Assess the morphology of the erythrocytes.
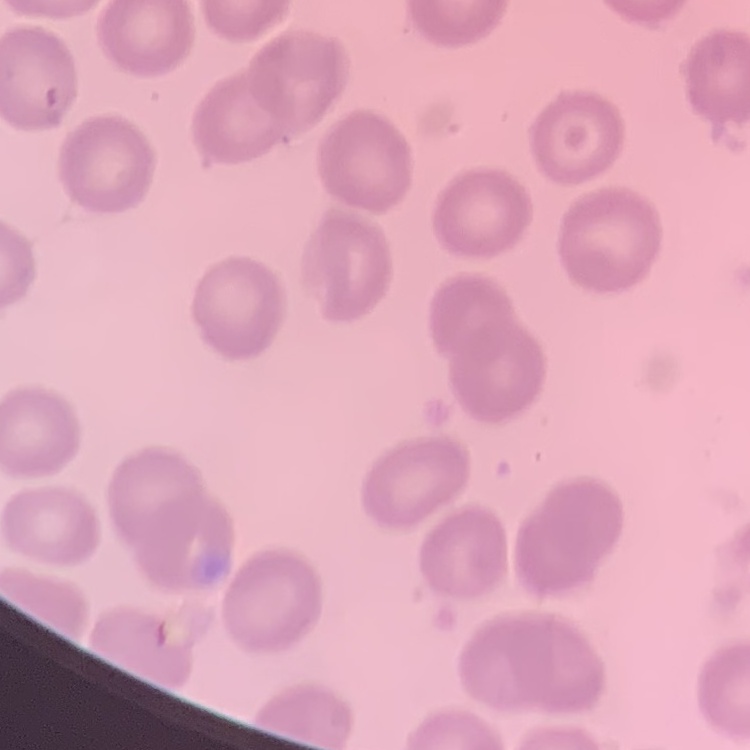
They show no rouleaux formation.

preparation: thin blood film
stain: Field's or Giemsa
image_type: square crop of a larger photomicrograph